Locate every Plasmodium parasite.
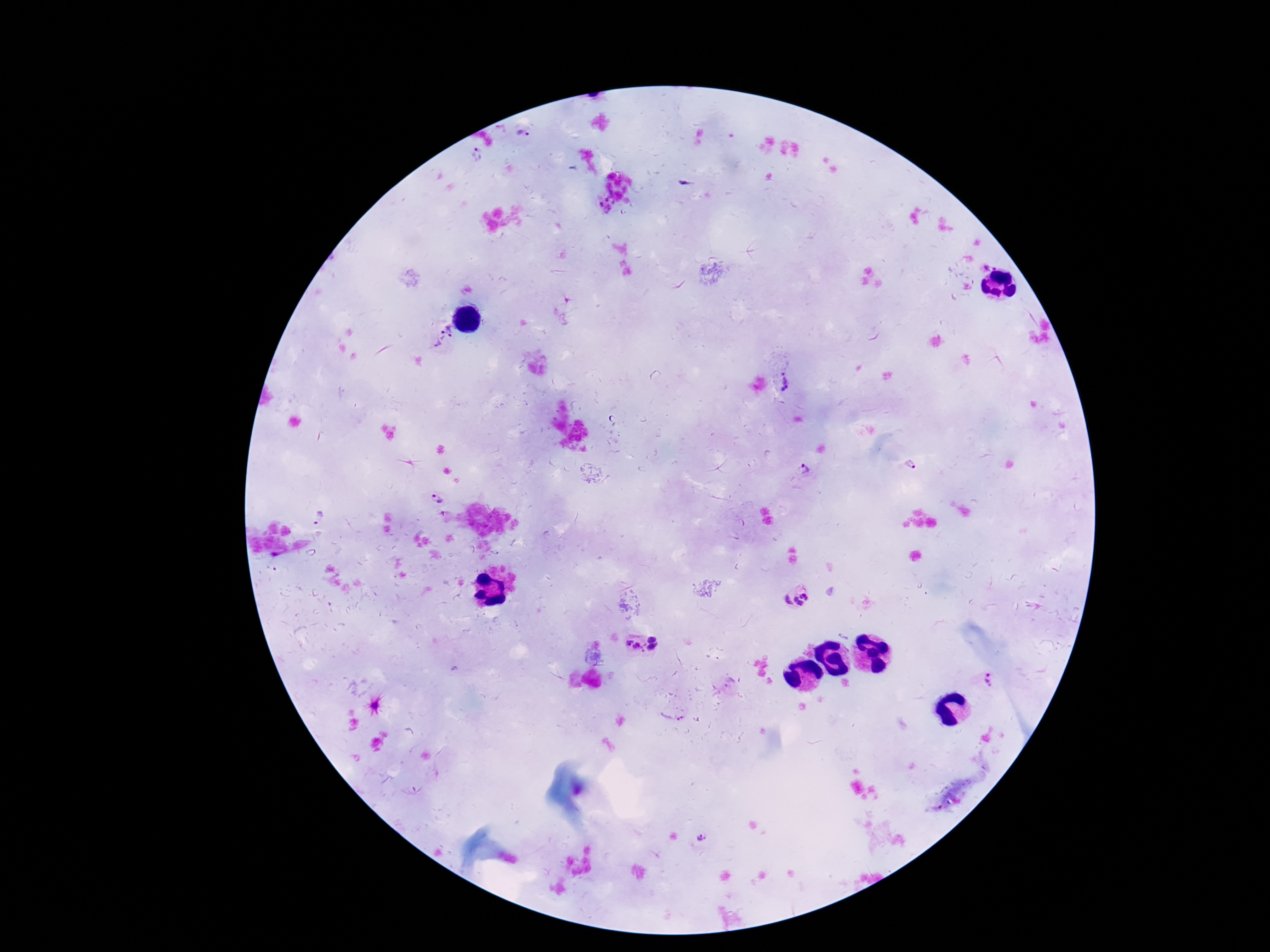

Approximate object centers, in pixels from the top-left corner.
Plasmodium parasites: (x=523, y=135), (x=477, y=155), (x=442, y=337), (x=791, y=382), (x=911, y=465), (x=806, y=472), (x=436, y=499), (x=320, y=518), (x=797, y=597), (x=652, y=638), (x=635, y=646), (x=653, y=648), (x=991, y=681), (x=672, y=720), (x=702, y=836).

Summary:
  - Field of view: single
  - Preparation: thick peripheral-blood smear
  - Image size: 1270×952 pixels
  - Patient malaria status: positive
  - Capture: smartphone camera through the microscope eyepiece
  - Magnification: 100x
  - Stain: Giemsa